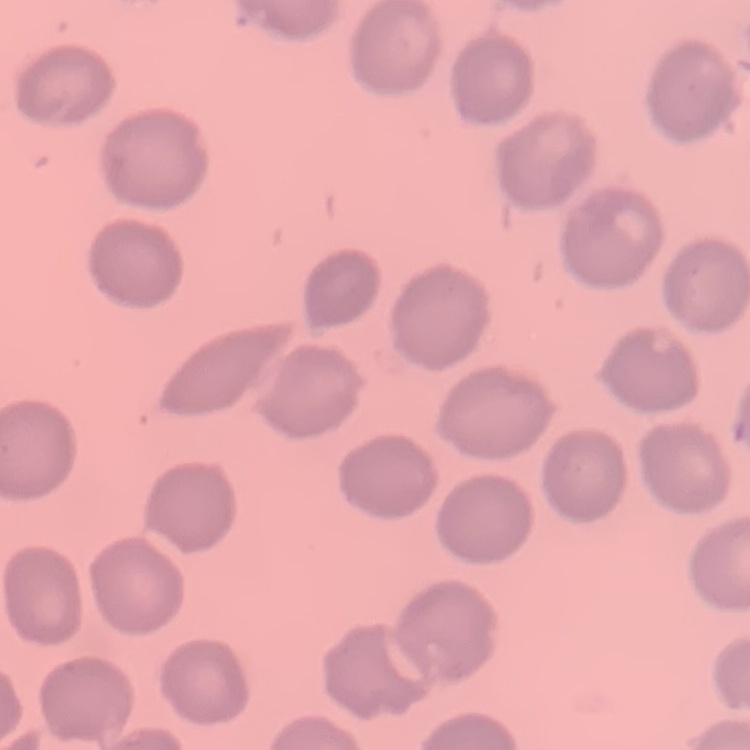
The erythrocytes show no rouleaux formation. Square crop of a larger photomicrograph. Field's or Giemsa stain. Thin blood film.